Identify the parasite.
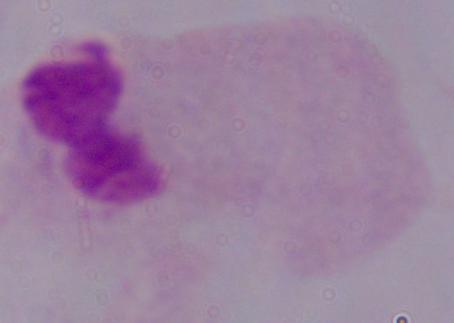
This is a trichomonad.

Summary:
  - Modality: photomicrograph
  - Magnification: 1000x